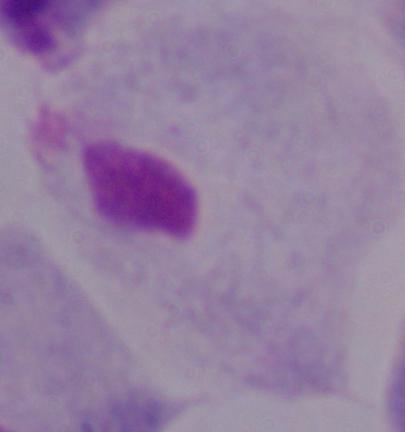

A trichomonad is shown. 1000x magnification. Photomicrograph.